Classify this cell by malaria status.
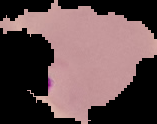

Parasitized.

{
  "preparation": "thin blood smear",
  "image_type": "segmented cell region with the area outside set to black",
  "image_size": "157×124 pixels"
}